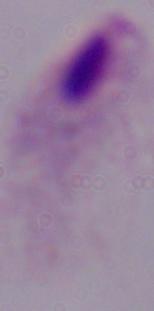

Summary:
  - Magnification: 1000x
  - Identification: trichomonad
  - Modality: photomicrograph